Outline each blood parasite and name the species.
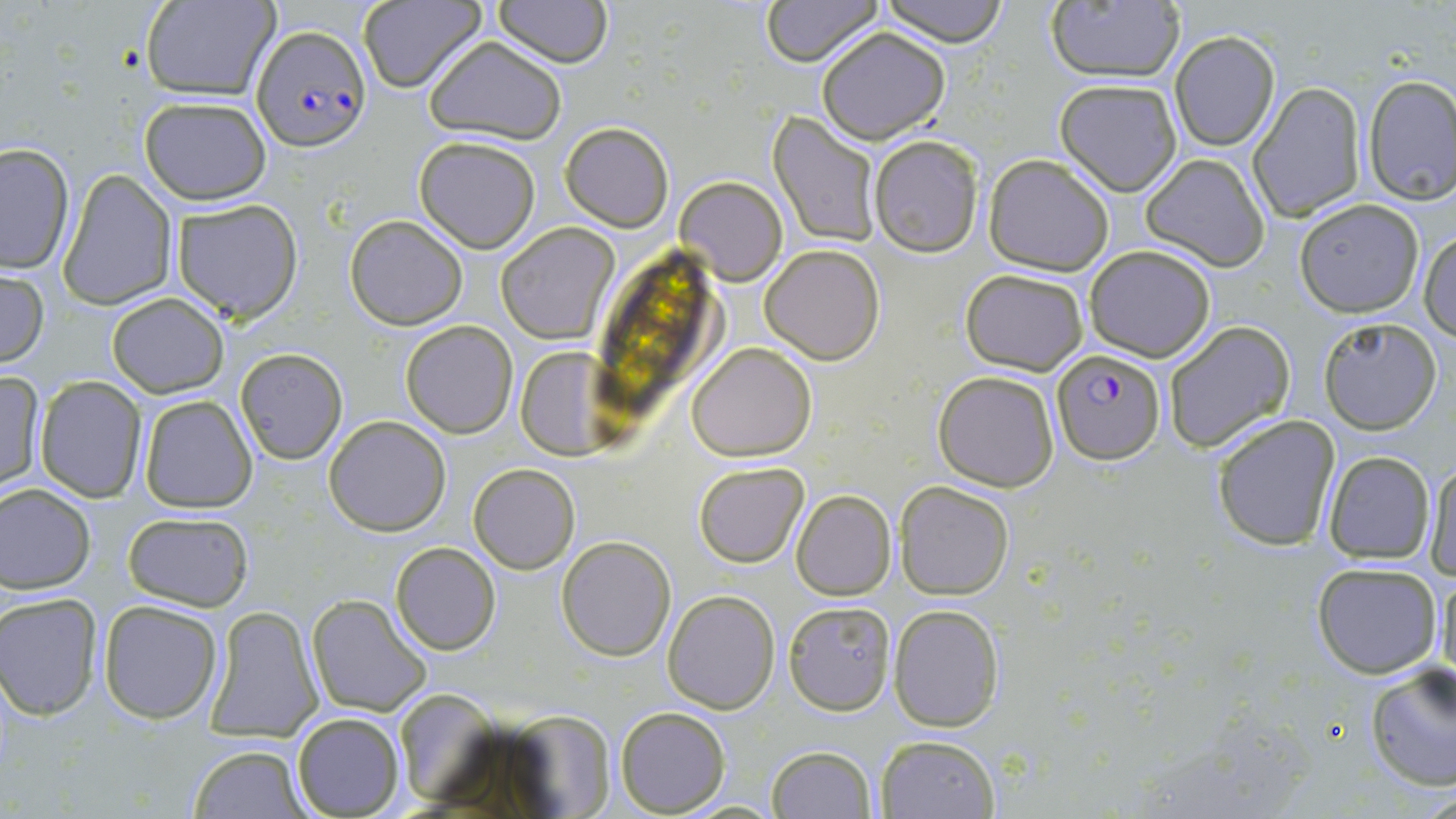
Approximate bounding boxes as named x1/y1/x2/y2 corners in pixels.
Plasmodium falciparum-infected red blood cells: (x1=252, y1=26, x2=370, y2=153), (x1=1050, y1=347, x2=1166, y2=463).
No Plasmodium ovale, Plasmodium malariae, Plasmodium vivax, Babesia divergens, or Trypanosoma brucei observed.

Uninfected red blood cell locations: (x1=140, y1=0, x2=278, y2=102), (x1=358, y1=0, x2=485, y2=92), (x1=494, y1=0, x2=613, y2=67), (x1=762, y1=0, x2=881, y2=66), (x1=880, y1=0, x2=1009, y2=47), (x1=1045, y1=3, x2=1185, y2=83), (x1=816, y1=26, x2=951, y2=144), (x1=1170, y1=31, x2=1280, y2=150), (x1=424, y1=36, x2=568, y2=145), (x1=1363, y1=73, x2=1456, y2=206), (x1=1053, y1=78, x2=1182, y2=196), (x1=1248, y1=82, x2=1366, y2=219), (x1=138, y1=96, x2=273, y2=205), (x1=769, y1=111, x2=882, y2=247), (x1=560, y1=121, x2=674, y2=231), (x1=414, y1=135, x2=541, y2=253), (x1=869, y1=135, x2=984, y2=257), (x1=0, y1=143, x2=75, y2=274), (x1=983, y1=153, x2=1115, y2=275), (x1=1141, y1=153, x2=1271, y2=272), (x1=58, y1=168, x2=177, y2=311), (x1=676, y1=175, x2=788, y2=285), (x1=170, y1=199, x2=303, y2=322), (x1=1294, y1=200, x2=1426, y2=318), (x1=345, y1=214, x2=468, y2=331), (x1=495, y1=223, x2=619, y2=345), (x1=1419, y1=230, x2=1456, y2=341), (x1=761, y1=244, x2=884, y2=364), (x1=1083, y1=245, x2=1216, y2=362), (x1=0, y1=268, x2=50, y2=371), (x1=960, y1=269, x2=1089, y2=374), (x1=105, y1=293, x2=229, y2=399), (x1=1317, y1=316, x2=1444, y2=433), (x1=400, y1=320, x2=519, y2=437), (x1=1161, y1=320, x2=1295, y2=453), (x1=687, y1=343, x2=817, y2=461), (x1=235, y1=347, x2=348, y2=465), (x1=514, y1=347, x2=614, y2=456), (x1=933, y1=369, x2=1061, y2=491), (x1=1, y1=371, x2=45, y2=493), (x1=34, y1=376, x2=148, y2=502), (x1=137, y1=394, x2=258, y2=513), (x1=324, y1=414, x2=450, y2=535), (x1=1210, y1=414, x2=1340, y2=551), (x1=1321, y1=451, x2=1435, y2=566), (x1=1424, y1=455, x2=1456, y2=582), (x1=693, y1=462, x2=809, y2=568), (x1=468, y1=464, x2=579, y2=574), (x1=895, y1=480, x2=1014, y2=600), (x1=0, y1=482, x2=96, y2=593), (x1=791, y1=490, x2=897, y2=600), (x1=122, y1=511, x2=255, y2=611), (x1=556, y1=534, x2=675, y2=660), (x1=390, y1=542, x2=500, y2=654), (x1=1312, y1=562, x2=1444, y2=679), (x1=1436, y1=564, x2=1455, y2=690), (x1=663, y1=590, x2=780, y2=712), (x1=1, y1=593, x2=104, y2=721), (x1=305, y1=593, x2=432, y2=717), (x1=97, y1=600, x2=224, y2=724), (x1=783, y1=601, x2=898, y2=716), (x1=204, y1=604, x2=323, y2=739), (x1=889, y1=604, x2=1004, y2=732), (x1=1363, y1=664, x2=1455, y2=792), (x1=615, y1=707, x2=730, y2=816), (x1=292, y1=713, x2=406, y2=819), (x1=876, y1=734, x2=999, y2=818), (x1=187, y1=743, x2=311, y2=818), (x1=766, y1=745, x2=877, y2=819). Slide-level diagnosis: Plasmodium falciparum. Thin blood film. Single field of view. Image is 1456×819 pixels. Captured at 1000x magnification. Light microscopy. May-Grünwald-Giemsa stain.